State which parasite is depicted.
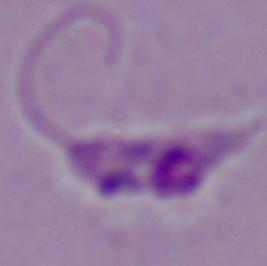

Leishmania.

modality = photomicrograph
magnification = 1000x